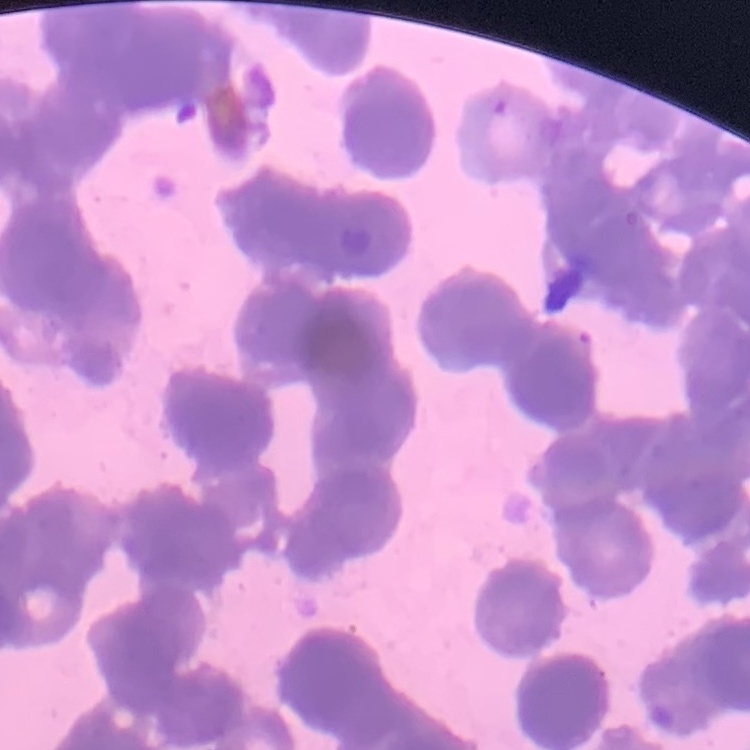
Summary:
  - Erythrocyte morphology: rouleaux formation
  - Preparation: thin blood film
  - Image type: one tile cut from a larger photomicrograph
  - Stain: Field's or Giemsa